Give the extent of all Plasmodium malariae-infected red blood cells.
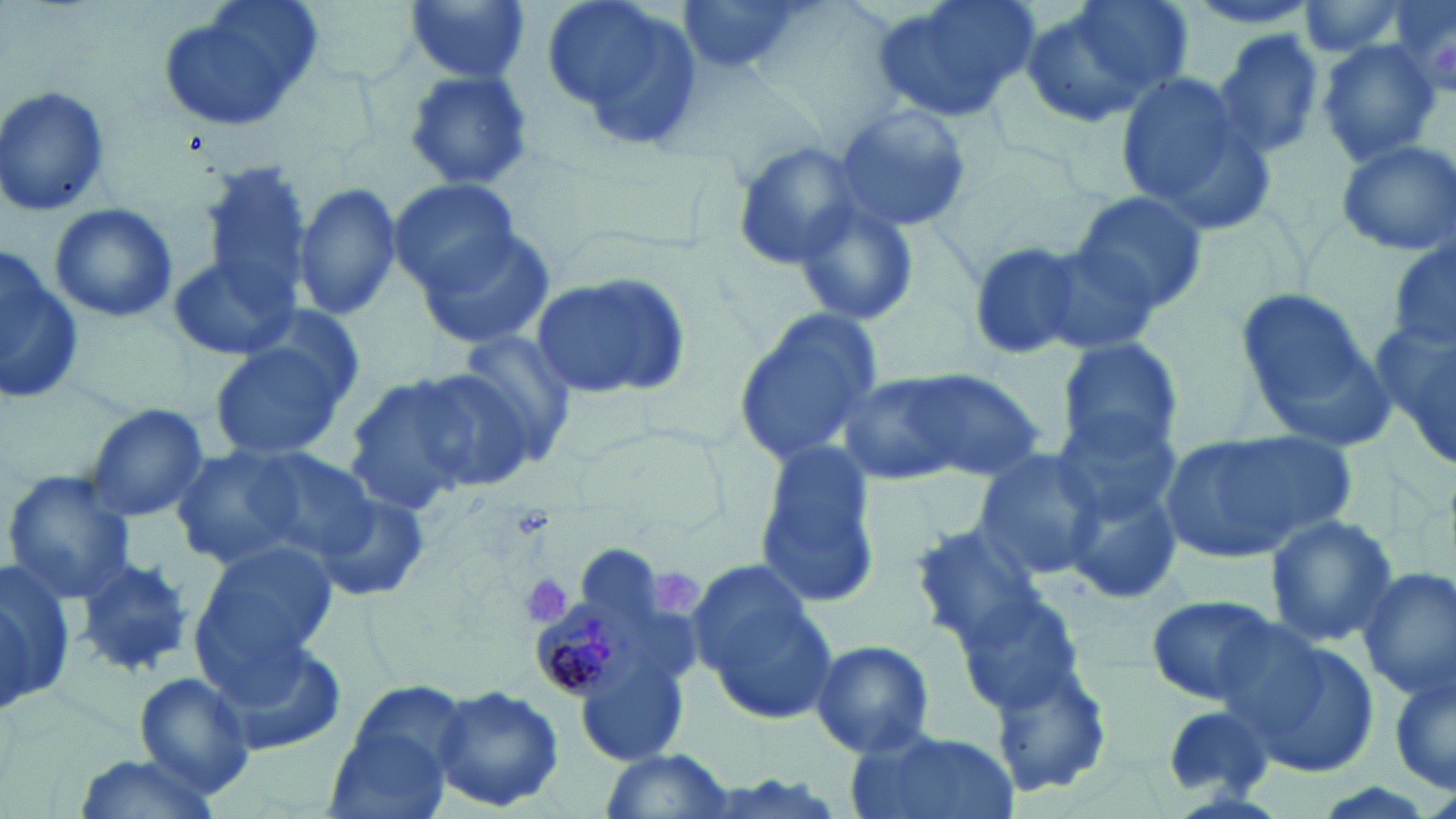
Approximate bounding boxes as named x1/y1/x2/y2 corners in pixels.
Plasmodium malariae-infected red blood cells: (x1=530, y1=604, x2=632, y2=700).

slide-level diagnosis = Plasmodium malariae
platelet locations = approximate bounding boxes as named x1/y1/x2/y2 corners in pixels: (x1=648, y1=570, x2=703, y2=619), (x1=522, y1=573, x2=574, y2=630)
stain = May-Grünwald-Giemsa
image size = 1456×819 pixels
magnification = 1000x
preparation = thin blood film
modality = light microscopy
uninfected red blood cell locations = approximate bounding boxes as named x1/y1/x2/y2 corners in pixels: (x1=154, y1=0, x2=325, y2=135), (x1=405, y1=0, x2=532, y2=85), (x1=542, y1=0, x2=705, y2=153), (x1=676, y1=0, x2=823, y2=81), (x1=872, y1=0, x2=1041, y2=123), (x1=1019, y1=0, x2=1188, y2=128), (x1=1177, y1=0, x2=1333, y2=31), (x1=1375, y1=0, x2=1456, y2=105), (x1=1292, y1=1, x2=1419, y2=59), (x1=1211, y1=30, x2=1325, y2=164), (x1=1313, y1=39, x2=1444, y2=165), (x1=402, y1=60, x2=540, y2=194), (x1=1112, y1=69, x2=1268, y2=223), (x1=1, y1=83, x2=113, y2=215), (x1=833, y1=102, x2=972, y2=233), (x1=1332, y1=138, x2=1456, y2=258), (x1=729, y1=140, x2=871, y2=271), (x1=199, y1=163, x2=315, y2=309), (x1=388, y1=179, x2=524, y2=293), (x1=295, y1=182, x2=402, y2=322), (x1=1071, y1=190, x2=1208, y2=318), (x1=788, y1=195, x2=922, y2=329), (x1=48, y1=204, x2=178, y2=324), (x1=412, y1=226, x2=557, y2=351), (x1=1037, y1=235, x2=1182, y2=356), (x1=969, y1=240, x2=1096, y2=361), (x1=0, y1=248, x2=88, y2=404), (x1=166, y1=254, x2=297, y2=362), (x1=529, y1=268, x2=693, y2=401), (x1=1232, y1=285, x2=1390, y2=438), (x1=1371, y1=306, x2=1456, y2=474), (x1=731, y1=309, x2=885, y2=470), (x1=453, y1=329, x2=580, y2=464), (x1=207, y1=331, x2=355, y2=463), (x1=1057, y1=337, x2=1184, y2=460), (x1=891, y1=367, x2=1048, y2=483), (x1=340, y1=371, x2=507, y2=513), (x1=837, y1=373, x2=969, y2=487), (x1=80, y1=402, x2=211, y2=525), (x1=1053, y1=407, x2=1182, y2=528), (x1=1158, y1=429, x2=1357, y2=564), (x1=170, y1=441, x2=381, y2=582), (x1=753, y1=443, x2=879, y2=609), (x1=970, y1=447, x2=1106, y2=579), (x1=2, y1=469, x2=140, y2=602), (x1=1062, y1=471, x2=1186, y2=610), (x1=309, y1=486, x2=433, y2=603), (x1=1263, y1=513, x2=1397, y2=649), (x1=908, y1=520, x2=1055, y2=652), (x1=189, y1=541, x2=337, y2=685), (x1=73, y1=556, x2=194, y2=677), (x1=0, y1=560, x2=73, y2=718), (x1=690, y1=563, x2=839, y2=724), (x1=1353, y1=568, x2=1456, y2=700), (x1=954, y1=587, x2=1089, y2=718), (x1=1145, y1=594, x2=1286, y2=708), (x1=1225, y1=627, x2=1378, y2=780), (x1=212, y1=637, x2=348, y2=757), (x1=805, y1=639, x2=936, y2=759), (x1=991, y1=661, x2=1115, y2=800), (x1=1387, y1=661, x2=1455, y2=799), (x1=578, y1=663, x2=685, y2=767), (x1=133, y1=671, x2=255, y2=801), (x1=325, y1=680, x2=469, y2=815), (x1=431, y1=684, x2=565, y2=813), (x1=1157, y1=702, x2=1274, y2=800), (x1=843, y1=728, x2=1018, y2=819), (x1=598, y1=751, x2=739, y2=819), (x1=70, y1=752, x2=226, y2=819)
field of view = one of a larger specimen